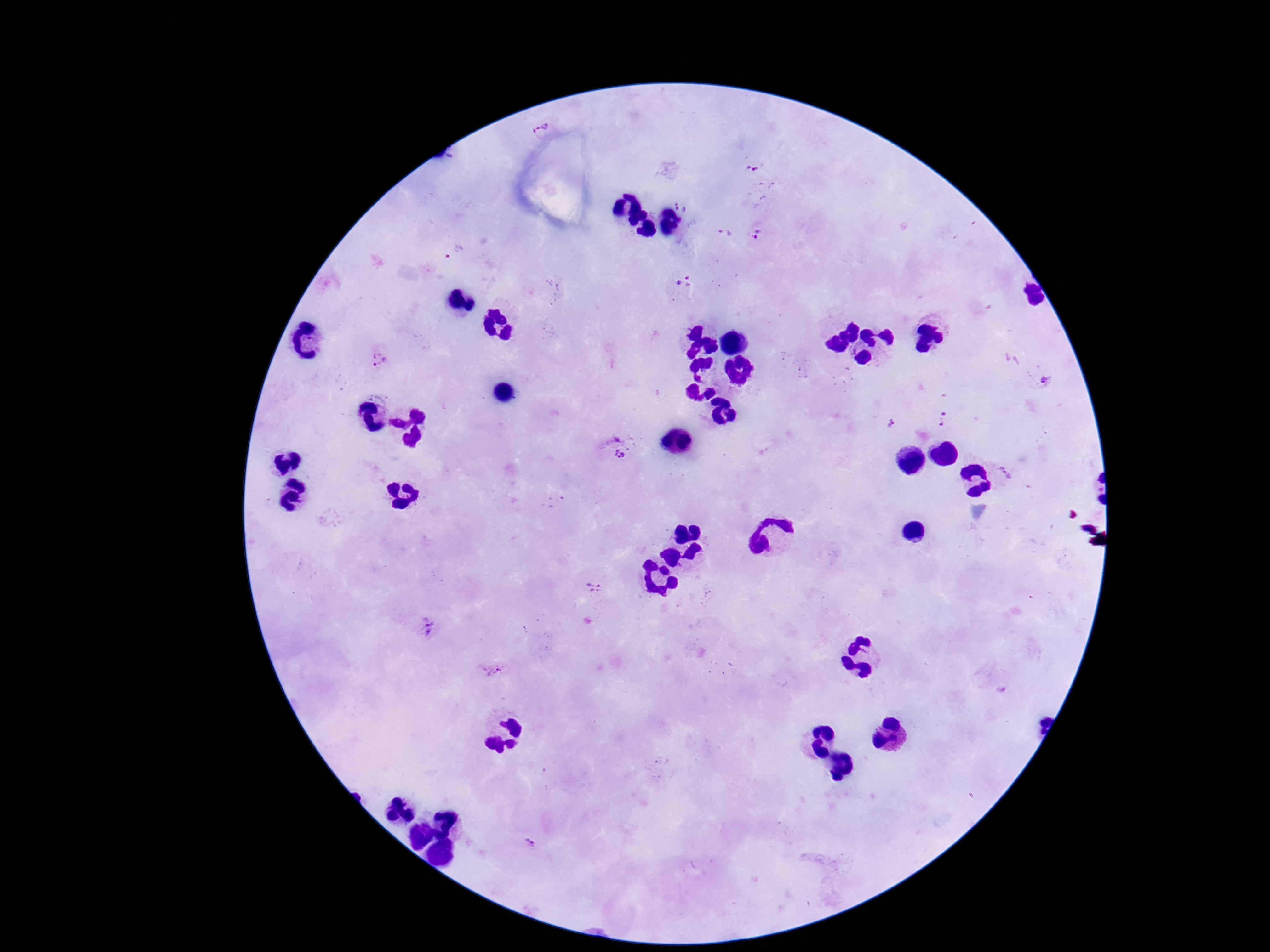
Approximate centers as [x, y] in pixels.
Summary:
  - Plasmodium parasite locations: [541, 117], [753, 166], [683, 203], [723, 233], [759, 235], [685, 281], [383, 359], [1045, 380], [945, 420], [890, 422], [621, 455], [1005, 471], [595, 585], [707, 595], [427, 628], [493, 669], [531, 845]
  - Preparation: thick blood smear
  - Capture: smartphone camera through the microscope eyepiece
  - Magnification: 100x
  - Field of view: one from this slide
  - Stain: Giemsa
  - Image size: 1270×952 pixels
  - Patient malaria status: positive